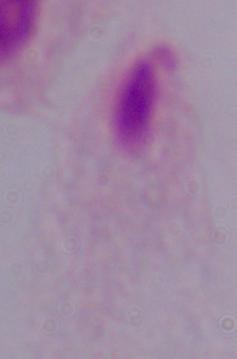 Captured at 1000x magnification. Photomicrograph. A trichomonad is seen.